Report the malaria status of this cell.
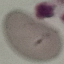

Uninfected.

Giemsa-stained preparation. Photographed with a smartphone camera at the microscope eyepiece. Cell patch, automatically extracted from a larger field of view and resized to 64 × 64 pixels. Thin blood smear.